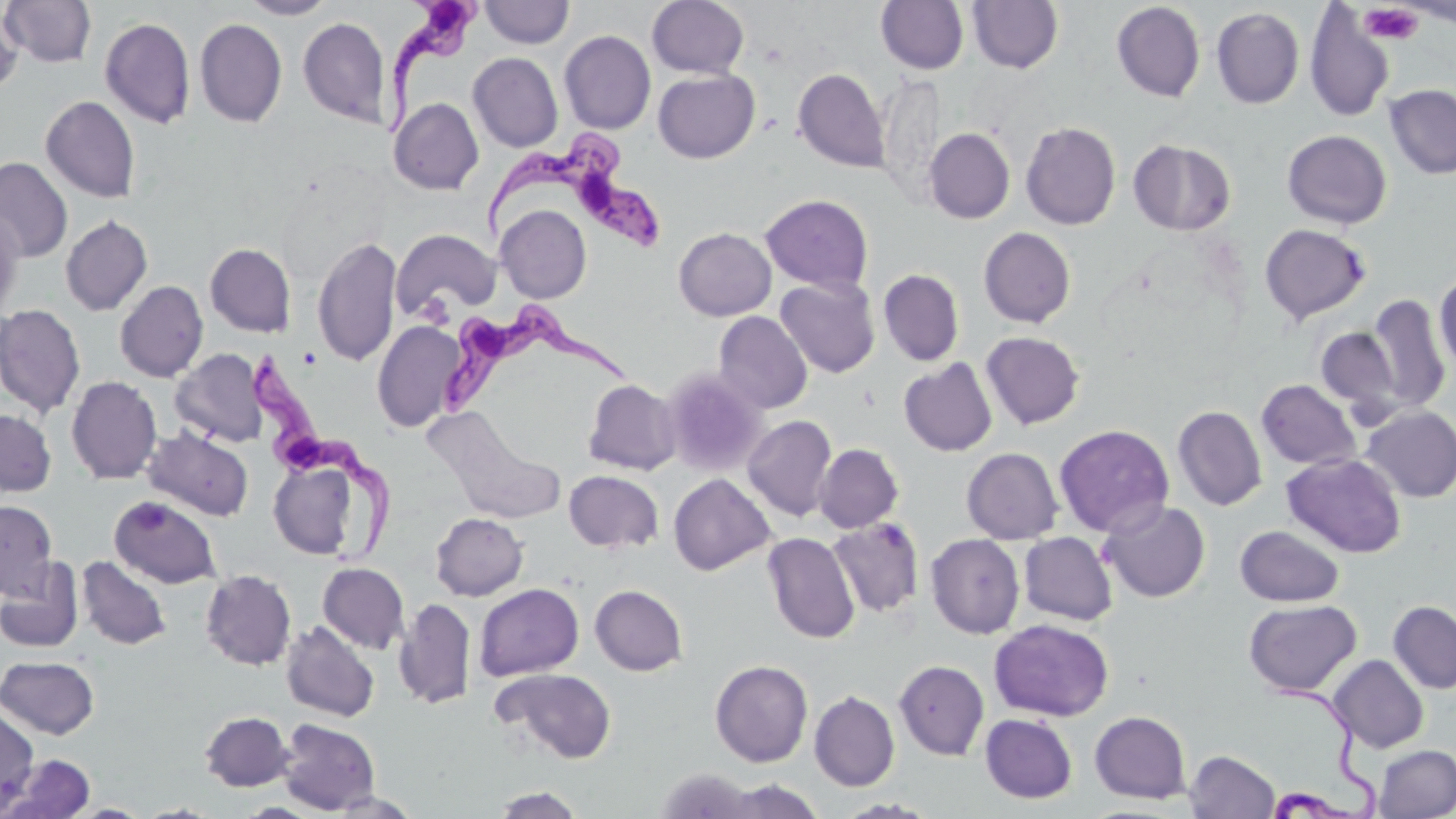
Summary:
  - Coordinate format: approximate bounding boxes as (x1,y1)-(x2,y2) corner pairs in pixels
  - Uninfected red blood cell locations: (1,0)-(97,67), (238,0)-(338,19), (647,0)-(749,79), (876,0)-(968,74), (967,0)-(1063,73), (480,1)-(574,48), (1111,2)-(1205,102), (0,4)-(24,98), (1304,5)-(1395,122), (1211,7)-(1305,109), (100,17)-(195,129), (298,17)-(391,128), (195,18)-(287,127), (559,30)-(656,134), (468,52)-(563,152), (793,68)-(890,173), (653,69)-(760,163), (1385,84)-(1456,179), (40,95)-(140,203), (389,97)-(483,195), (1021,122)-(1121,230), (925,128)-(1015,224), (1282,129)-(1392,229), (1129,138)-(1236,235), (0,157)-(73,261), (760,194)-(873,293), (496,205)-(591,303), (0,208)-(25,322), (60,215)-(153,316), (1259,223)-(1371,325), (673,227)-(776,321), (978,227)-(1076,328), (391,229)-(501,320), (312,235)-(401,367), (205,243)-(296,337), (878,269)-(965,366), (1433,273)-(1456,375), (775,277)-(880,378), (115,280)-(208,382), (1367,294)-(1451,414), (0,304)-(85,419), (713,310)-(813,414), (372,322)-(466,433), (1316,326)-(1404,421), (980,331)-(1085,430), (170,349)-(268,447), (899,358)-(998,457), (661,367)-(767,477), (66,376)-(162,485), (584,379)-(681,475), (1257,379)-(1360,470), (1172,405)-(1267,510), (1359,405)-(1456,502), (0,409)-(57,496), (742,415)-(837,521), (435,418)-(568,522), (1054,423)-(1174,537), (143,425)-(254,521), (814,443)-(903,533), (961,447)-(1063,544), (1282,453)-(1406,558), (268,456)-(366,562), (563,470)-(664,553), (668,473)-(776,576), (109,495)-(221,589), (0,500)-(58,600), (1099,500)-(1211,602), (431,512)-(528,600), (827,517)-(925,617), (1235,525)-(1345,606), (762,532)-(859,643), (1019,532)-(1117,625), (925,533)-(1025,639), (77,555)-(172,651), (0,558)-(84,653), (318,562)-(410,653), (200,569)-(296,670), (474,583)-(584,681), (590,584)-(688,676), (394,598)-(476,710), (1244,599)-(1361,697), (1388,600)-(1456,694), (990,618)-(1114,721), (281,620)-(380,722), (1327,654)-(1429,752), (1,655)-(99,739), (710,660)-(813,768), (894,660)-(989,760), (492,667)-(617,763), (809,690)-(900,791), (0,704)-(40,813), (200,711)-(295,792), (1090,711)-(1191,804), (980,713)-(1077,803), (277,718)-(381,814), (1374,745)-(1456,818), (1185,750)-(1280,819), (3,754)-(95,819), (655,767)-(761,817), (715,778)-(827,818), (491,785)-(584,818), (326,790)-(424,817), (134,802)-(223,818), (66,803)-(152,818)
  - Platelet locations: (1358,3)-(1424,45)
  - Trypanosoma brucei locations: (381,0)-(488,141), (483,136)-(664,255), (442,308)-(638,414), (249,351)-(387,557)
  - Slide-level diagnosis: Trypanosoma brucei
  - Field of view: single
  - Magnification: 1000x
  - Modality: optical microscopy
  - Preparation: thin blood film
  - Stain: May-Grünwald-Giemsa
  - Image size: 1456×819 pixels